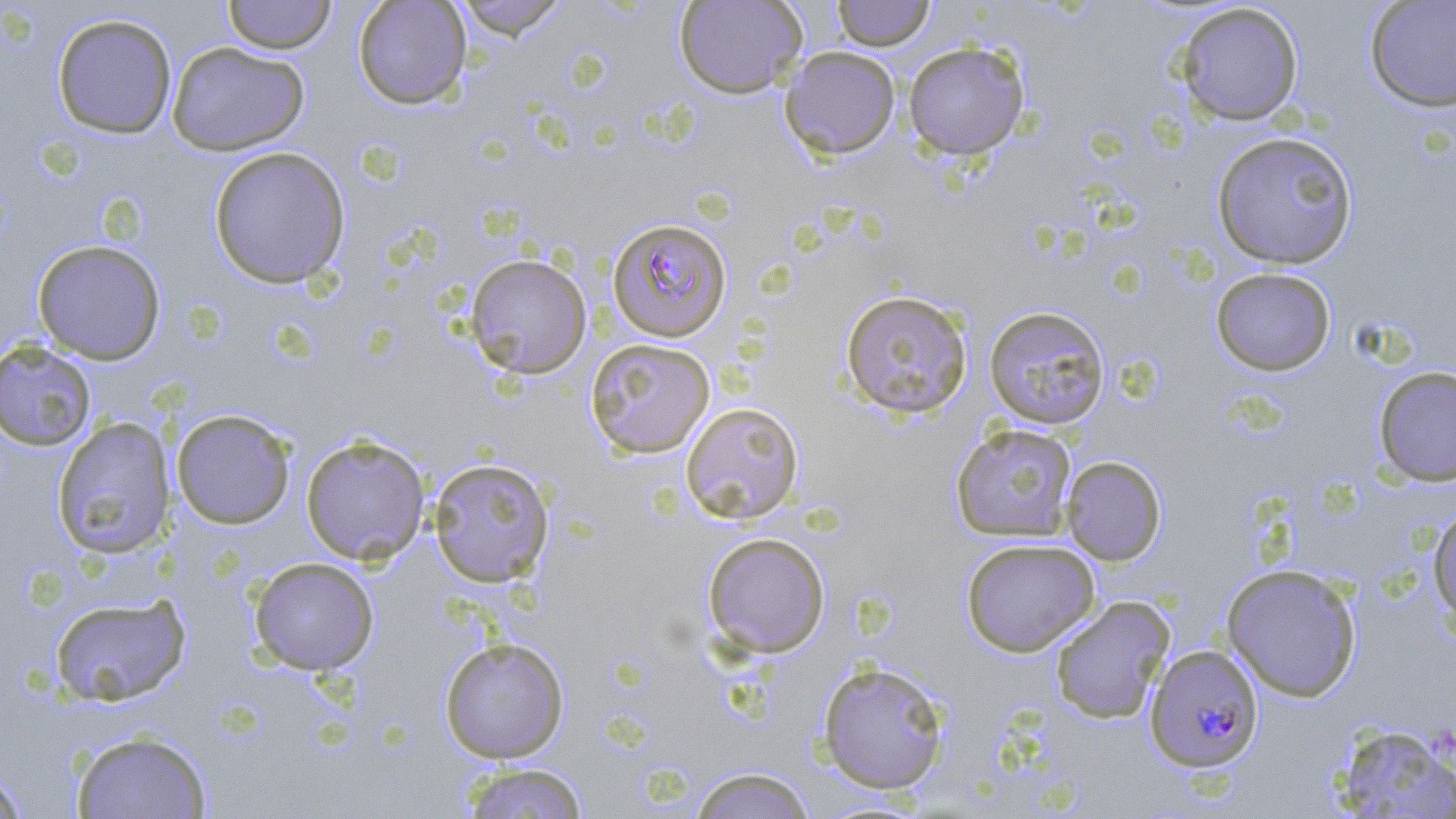

Approximate bounding boxes as (x1,y1)-(x2,y2) corner pairs in pixels. Plasmodium falciparum-infected red blood cell locations: (606,217)-(732,342), (1145,644)-(1264,773). Uninfected red blood cell locations: (222,0)-(337,54), (352,0)-(472,110), (453,0)-(569,40), (674,0)-(807,99), (831,0)-(936,51), (1364,0)-(1456,111), (1175,3)-(1304,125), (51,13)-(178,139), (167,42)-(309,156), (903,42)-(1029,160), (780,46)-(900,159), (1211,130)-(1359,269), (208,146)-(351,289), (32,239)-(166,364), (465,254)-(592,379), (1210,267)-(1336,376), (839,289)-(973,419), (984,305)-(1111,429), (585,338)-(715,458), (0,341)-(97,451), (1373,365)-(1456,486), (680,402)-(804,524), (170,408)-(297,529), (51,416)-(176,560), (951,423)-(1078,542), (301,434)-(431,565), (1061,455)-(1166,566), (428,457)-(554,587), (1427,502)-(1456,628), (702,531)-(831,658), (960,538)-(1100,657), (249,557)-(379,675), (1221,563)-(1363,702), (49,593)-(191,707), (1049,595)-(1175,724), (439,637)-(569,763), (817,661)-(951,795), (1331,723)-(1456,818), (71,730)-(212,819), (459,762)-(590,819), (0,766)-(30,818), (688,766)-(817,818). Slide-level diagnosis: Plasmodium falciparum. Captured at 1000x magnification. Light microscopy. Single field of view. Image is 1456×819 pixels. May-Grünwald-Giemsa-stained preparation. Thin blood film.